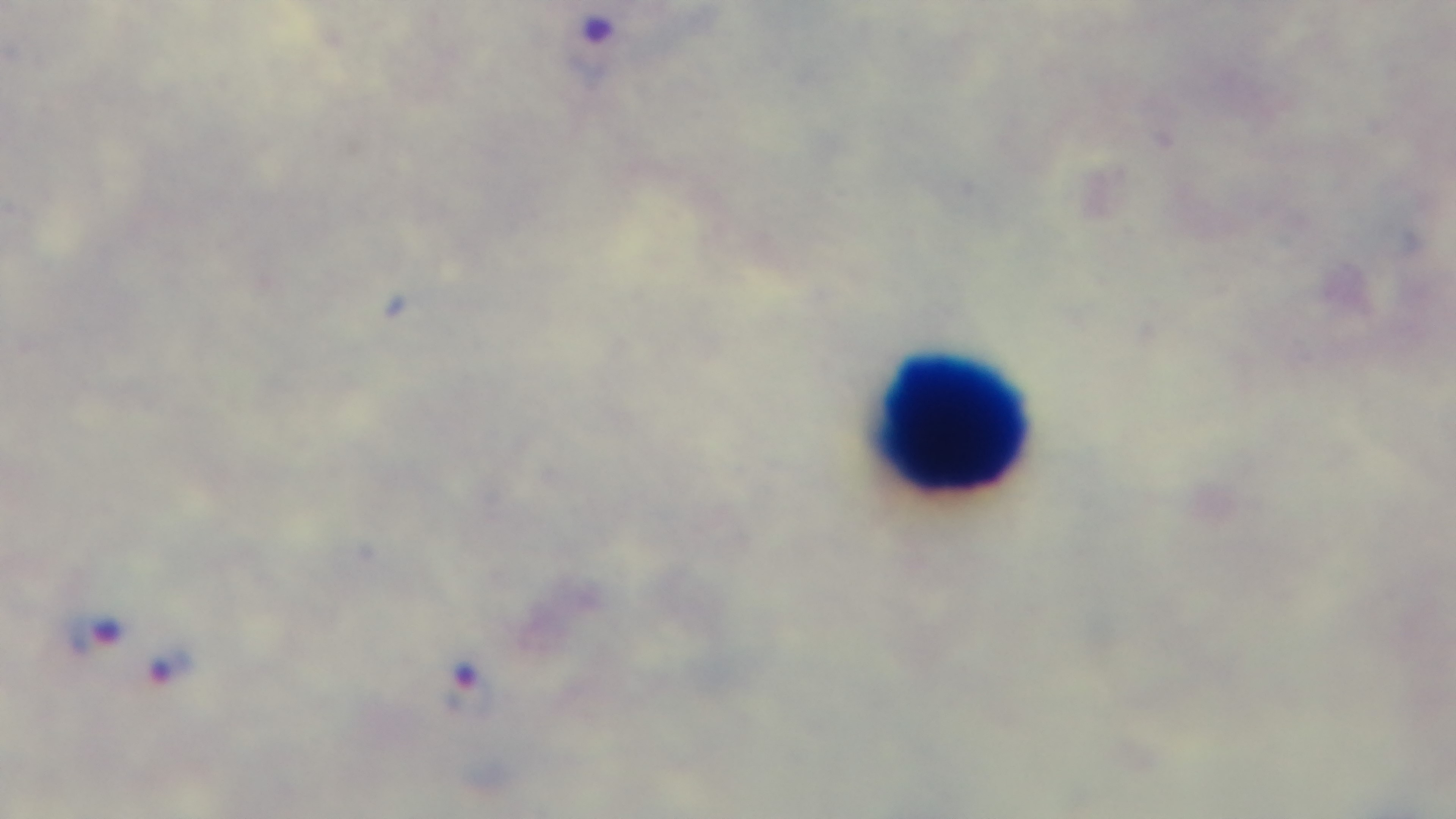
Summary:
  - Field of view: single
  - Objective: 100x oil immersion
  - Modality: light microscopy
  - Preparation: thick
  - Stain: Giemsa
  - Malaria status: positive
  - Capture: mounted 4K digital camera